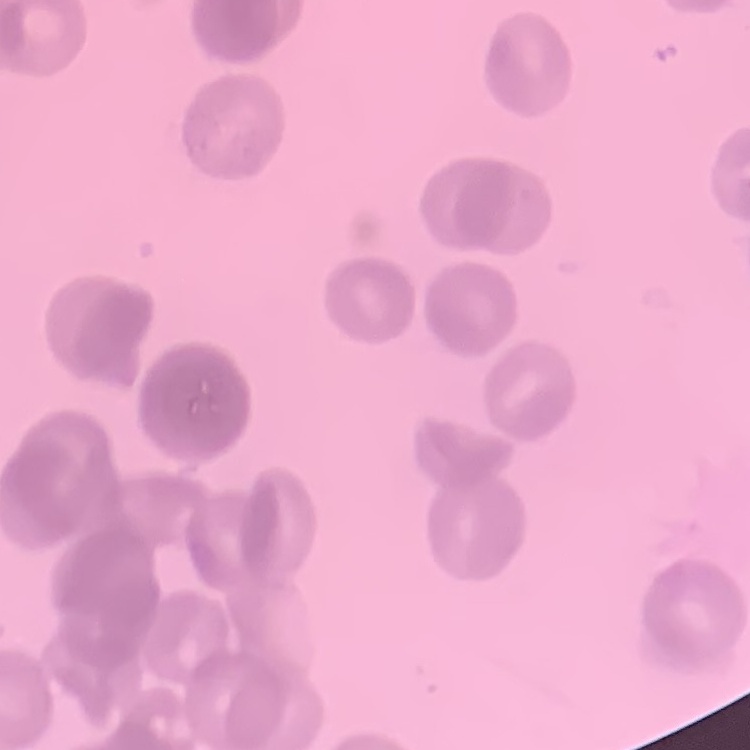

erythrocyte morphology = rouleaux formation
stain = Field's or Giemsa
preparation = thin blood smear
image type = square crop of a larger photomicrograph